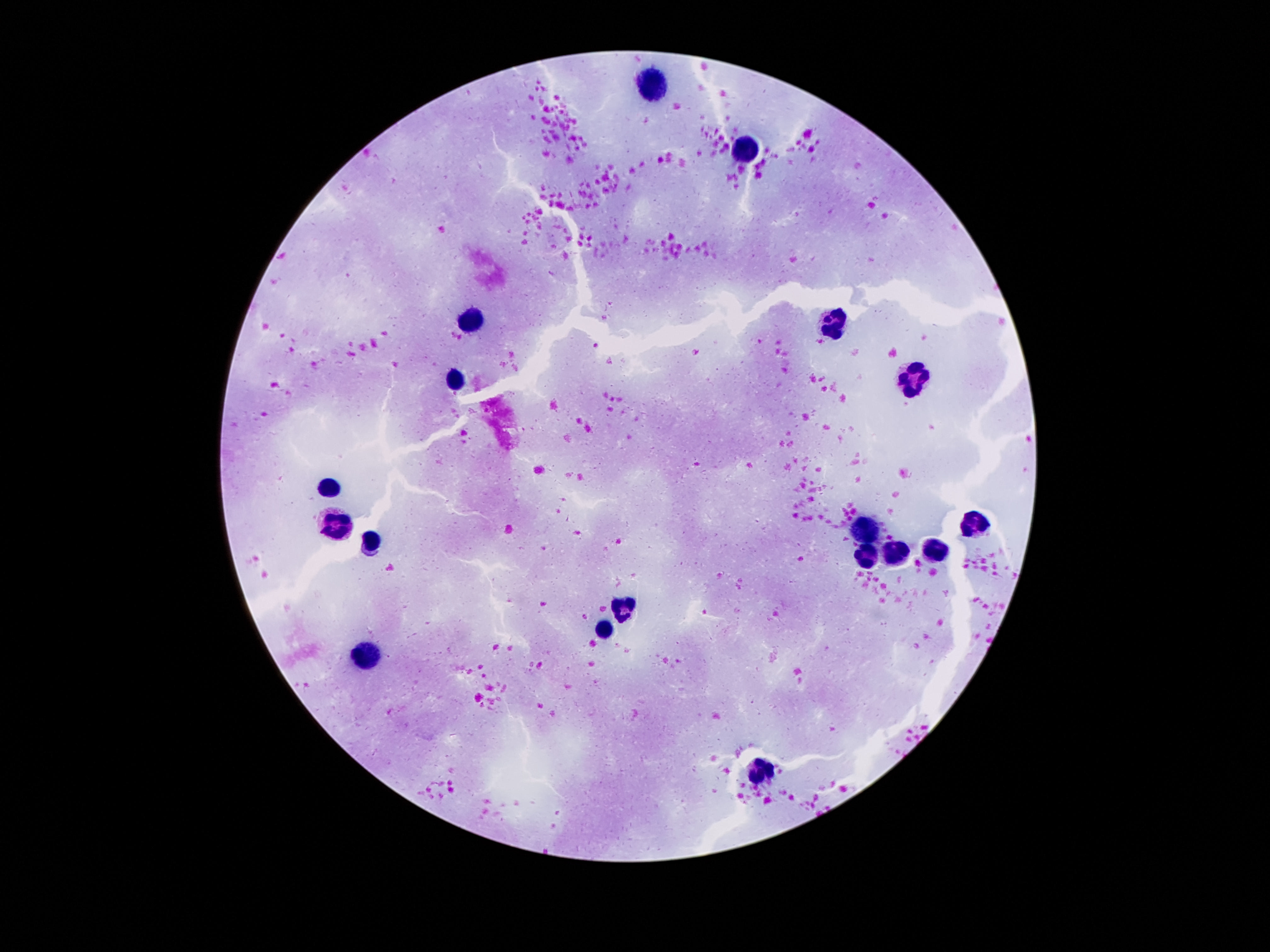

capture = smartphone camera through the microscope eyepiece
patient malaria status = uninfected
preparation = thick blood film
image size = 1270×952 pixels
field of view = single
leukocyte locations = approximate centers as {x, y} in pixels: {655, 87}, {749, 149}, {473, 321}, {831, 326}, {915, 378}, {457, 380}, {330, 487}, {334, 522}, {973, 524}, {868, 528}, {371, 544}, {932, 553}, {895, 554}, {866, 557}, {627, 608}, {604, 630}, {364, 655}, {762, 770}
magnification = 100x
stain = Giemsa